State which parasite is depicted.
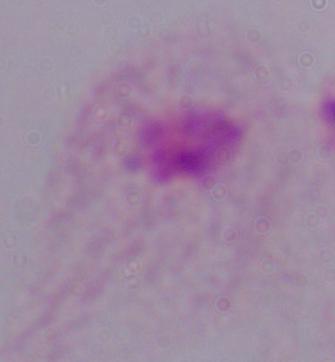

A trichomonad.

{
  "modality": "photomicrograph",
  "magnification": "1000x"
}